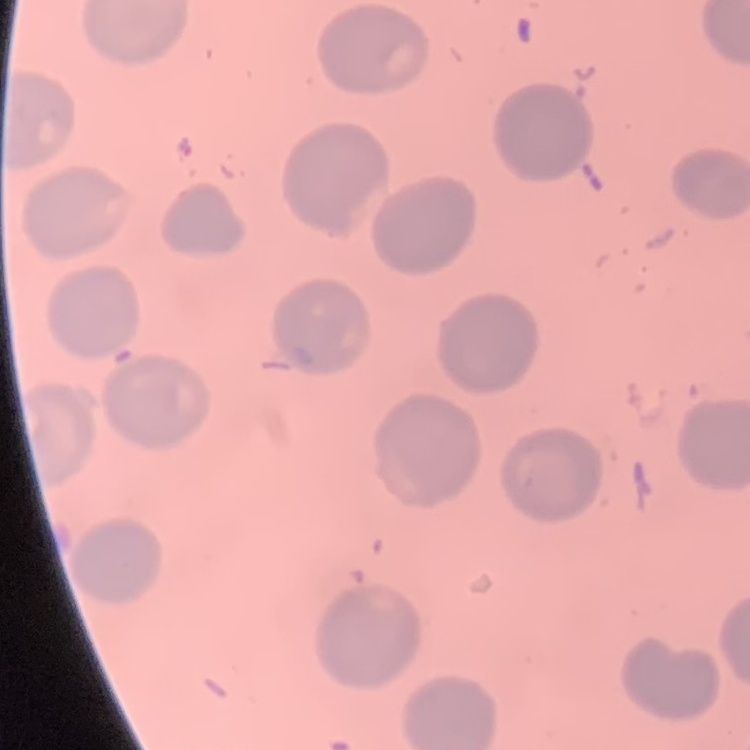
Summary:
  - Erythrocyte morphology: no rouleaux formation
  - Stain: Field's or Giemsa
  - Preparation: thin blood smear
  - Image type: one tile cut from a larger photomicrograph